Outline each blood parasite and name the species.
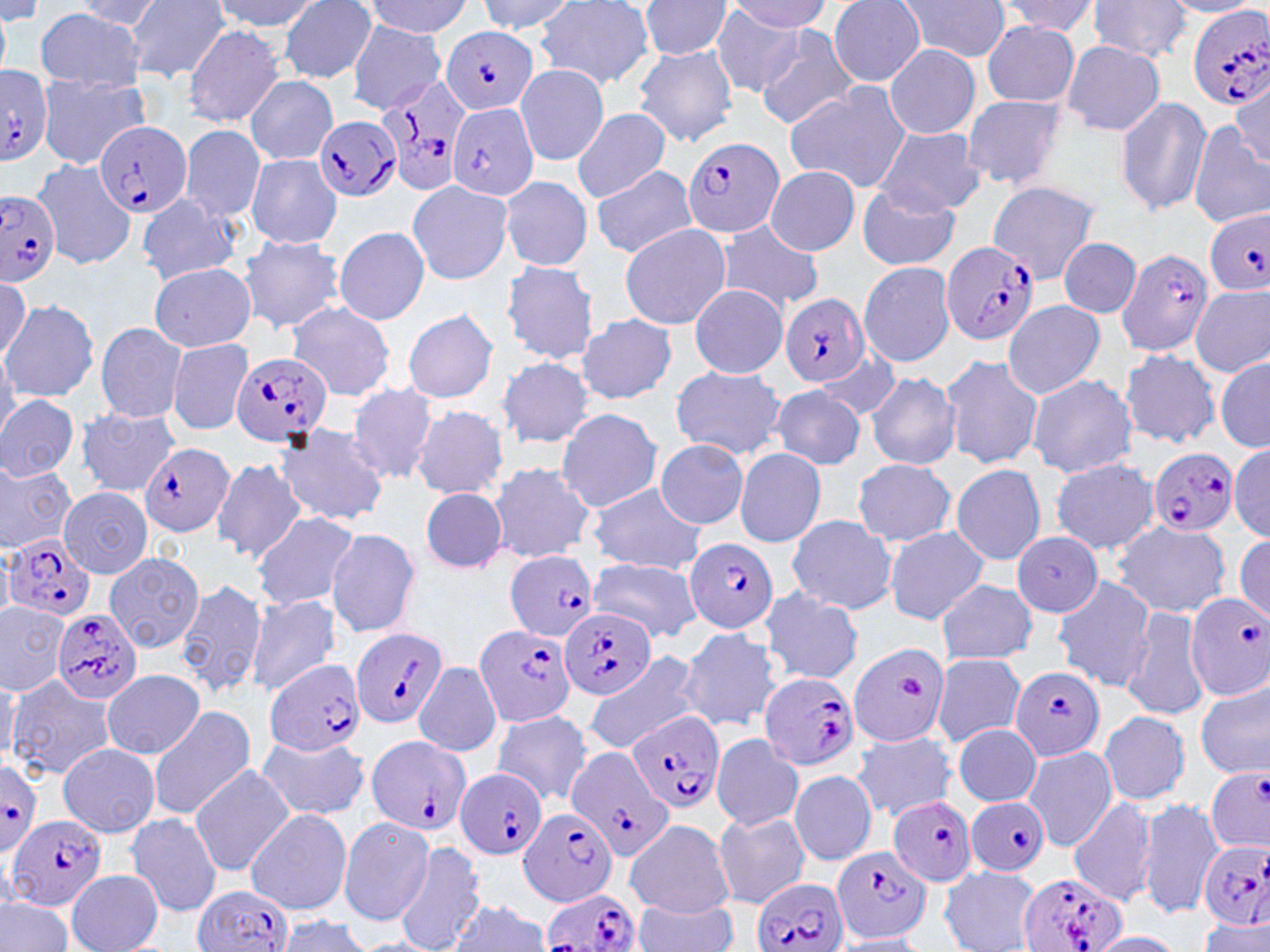

Approximate bounding boxes as (x1,y1)-(x2,y2) corner pairs in pixels.
Plasmodium falciparum-infected red blood cells: (1187,5)-(1270,112), (439,25)-(537,116), (0,67)-(53,163), (375,71)-(474,196), (445,101)-(540,202), (315,115)-(401,202), (95,119)-(192,218), (680,137)-(784,238), (0,190)-(61,286), (1203,209)-(1270,295), (943,242)-(1041,346), (1117,247)-(1214,357), (781,293)-(872,388), (229,351)-(334,449), (139,442)-(233,536), (1148,449)-(1236,536), (5,533)-(98,623), (684,538)-(780,633), (504,550)-(600,639), (1186,592)-(1270,700), (562,607)-(656,701), (50,609)-(142,707), (473,624)-(576,728), (350,627)-(450,730), (265,658)-(365,756), (1011,665)-(1106,761), (760,671)-(860,772), (626,711)-(724,815), (365,735)-(470,838), (565,746)-(671,861), (0,761)-(43,852), (1204,764)-(1270,856), (457,769)-(547,860), (966,795)-(1050,876), (888,797)-(978,888), (518,807)-(617,907), (7,814)-(106,914), (1198,839)-(1270,929), (833,845)-(932,945), (1017,871)-(1125,952), (755,877)-(847,952), (193,884)-(295,952), (540,886)-(641,952).
No Plasmodium ovale, Plasmodium malariae, Plasmodium vivax, Babesia divergens, or Trypanosoma brucei observed.

Platelet locations: (899,674)-(926,703). Uninfected red blood cell locations: (213,0)-(318,31), (475,0)-(577,34), (535,0)-(656,90), (638,0)-(732,60), (893,0)-(1011,63), (1085,0)-(1193,62), (75,1)-(167,29), (125,1)-(230,80), (278,1)-(377,82), (364,1)-(473,37), (724,1)-(830,36), (829,1)-(926,86), (995,1)-(1104,37), (1160,1)-(1263,19), (0,2)-(42,28), (0,3)-(11,81), (709,6)-(806,96), (36,7)-(145,92), (348,22)-(448,112), (980,22)-(1081,107), (183,24)-(285,126), (753,26)-(859,128), (1060,40)-(1166,136), (633,44)-(738,146), (884,46)-(981,138), (515,63)-(607,167), (1077,65)-(1189,205), (36,74)-(150,168), (246,75)-(338,166), (1231,79)-(1269,169), (784,83)-(912,193), (959,94)-(1071,190), (1114,96)-(1211,216), (571,107)-(671,203), (1188,119)-(1270,229), (177,124)-(266,222), (874,126)-(987,217), (245,153)-(342,250), (31,157)-(135,270), (590,163)-(699,260), (764,166)-(860,255), (499,175)-(593,271), (406,179)-(514,286), (988,180)-(1100,283), (856,187)-(961,272), (137,193)-(239,285), (713,222)-(823,312), (618,224)-(732,330), (334,225)-(430,326), (238,236)-(346,334), (1058,237)-(1141,318), (501,260)-(600,363), (148,262)-(256,351), (858,262)-(955,367), (0,276)-(29,363), (1190,283)-(1270,378), (688,284)-(788,378), (2,299)-(98,403), (1003,301)-(1105,399), (288,302)-(395,401), (402,309)-(500,404), (578,315)-(677,405), (95,322)-(188,424), (166,338)-(255,435), (1119,348)-(1219,448), (814,349)-(901,423), (940,354)-(1044,470), (497,356)-(595,450), (1215,357)-(1269,452), (668,364)-(786,460), (865,371)-(961,470), (1027,373)-(1139,478), (346,383)-(438,486), (771,385)-(866,470), (0,393)-(78,482), (410,405)-(509,501), (72,407)-(181,499), (554,408)-(663,514), (273,424)-(390,525), (655,439)-(749,530), (1230,444)-(1270,541), (734,448)-(827,547), (0,458)-(76,552), (1049,458)-(1159,556), (211,459)-(309,565), (852,460)-(958,547), (487,462)-(596,564), (864,462)-(971,622), (950,463)-(1047,565), (587,484)-(706,573), (59,487)-(153,577), (420,487)-(507,573), (252,512)-(360,613), (786,514)-(897,614), (1110,520)-(1232,618), (883,526)-(990,624), (325,527)-(420,638), (1014,533)-(1102,616), (1233,534)-(1270,626), (102,553)-(203,653), (587,558)-(701,643), (1052,575)-(1155,690), (172,578)-(267,701), (936,578)-(1036,666), (760,588)-(863,684), (245,593)-(342,696), (0,601)-(70,695), (1121,607)-(1210,723), (676,626)-(779,733), (849,639)-(947,747), (582,650)-(705,757), (930,653)-(1026,748), (414,661)-(501,757), (0,669)-(20,767), (102,669)-(204,760), (5,674)-(111,781), (1195,682)-(1270,778), (145,705)-(258,821), (489,709)-(593,806), (1098,709)-(1190,805), (953,724)-(1041,805), (852,730)-(956,822), (711,732)-(802,831), (255,735)-(371,821), (58,744)-(160,838), (1023,747)-(1117,851), (188,764)-(294,875), (789,767)-(879,866), (1068,795)-(1160,906), (1138,796)-(1222,920), (246,809)-(352,914), (125,811)-(223,917), (711,811)-(811,909), (338,815)-(435,925), (625,819)-(735,917), (391,842)-(487,952), (940,866)-(1041,952), (67,869)-(164,951), (0,896)-(75,952), (447,899)-(550,952), (633,899)-(740,952), (274,915)-(374,951), (1197,918)-(1269,952), (1086,932)-(1186,952), (831,934)-(930,952). Slide-level diagnosis: Plasmodium falciparum. May-Grünwald-Giemsa stain. Image is 1270×952 pixels. 1000x magnification. One field of a larger specimen. Thin blood film. Optical microscopy.